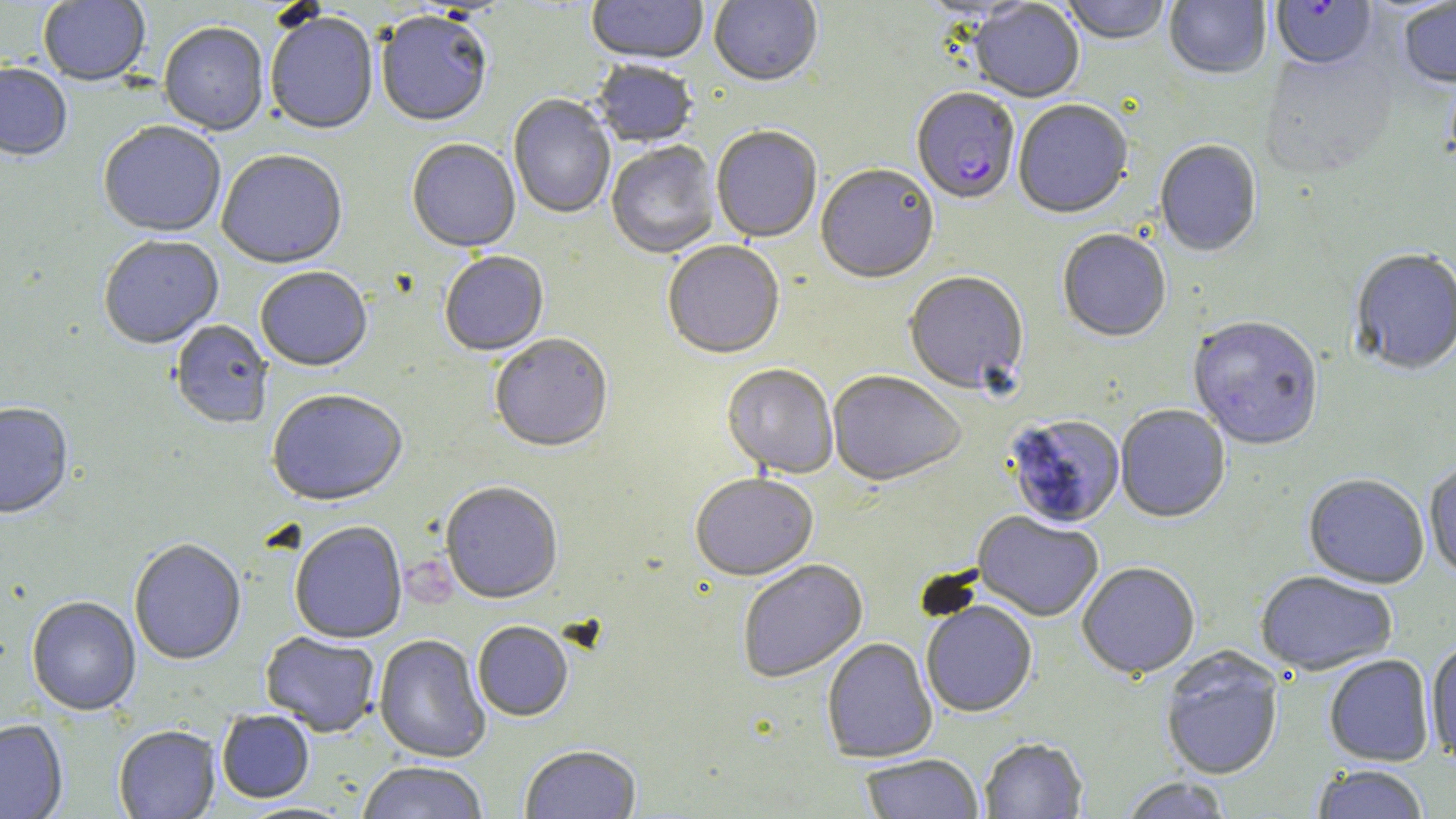
Summary:
  - Coordinate format: approximate bounding boxes as (x1,y1)-(x2,y2) corner pairs in pixels
  - Platelet locations: (403,557)-(456,612)
  - Plasmodium falciparum-infected red blood cell locations: (1271,0)-(1377,73), (912,89)-(1020,207)
  - Uninfected red blood cell locations: (38,0)-(151,88), (587,0)-(708,67), (708,0)-(823,89), (915,0)-(1040,22), (1059,0)-(1171,47), (1164,0)-(1271,81), (969,1)-(1084,104), (1399,2)-(1456,89), (376,14)-(492,129), (265,15)-(378,137), (158,24)-(269,138), (1258,51)-(1400,183), (592,62)-(698,149), (0,64)-(72,163), (508,95)-(615,220), (1013,102)-(1133,221), (98,123)-(226,239), (711,127)-(822,244), (407,140)-(520,255), (1155,141)-(1262,259), (606,142)-(720,260), (216,152)-(347,272), (816,166)-(939,286), (1057,231)-(1171,344), (99,237)-(224,351), (662,243)-(785,361), (1349,251)-(1456,378), (439,253)-(549,358), (255,269)-(373,374), (903,273)-(1029,396), (1187,318)-(1323,453), (170,321)-(273,430), (490,336)-(613,455), (721,366)-(838,480), (827,372)-(965,489), (267,392)-(408,509), (0,405)-(74,521), (1116,406)-(1230,525), (1004,415)-(1125,530), (1423,464)-(1456,580), (690,475)-(818,583), (1303,475)-(1428,591), (440,484)-(563,607), (972,512)-(1103,623), (290,523)-(408,645), (129,540)-(246,666), (738,561)-(868,685), (1078,564)-(1200,682), (1255,572)-(1397,676), (26,598)-(141,717), (920,603)-(1037,719), (473,623)-(573,723), (261,632)-(380,738), (374,635)-(489,763), (822,639)-(938,764), (1426,641)-(1456,765), (1160,647)-(1285,782), (1324,656)-(1435,767), (217,711)-(315,804), (0,720)-(68,819), (113,727)-(220,819), (979,739)-(1088,818), (520,746)-(642,819), (860,755)-(984,819), (356,763)-(489,819), (1312,765)-(1429,819), (1119,777)-(1234,819)
  - Slide-level diagnosis: Plasmodium falciparum
  - Image size: 1456×819 pixels
  - Preparation: thin blood smear
  - Modality: light microscopy
  - Field of view: single
  - Magnification: 1000x
  - Stain: May-Grünwald-Giemsa